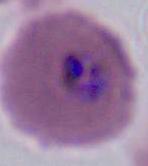
A Plasmodium parasite is seen. 400x or 1000x magnification. Micrograph.